Comment on the morphology of the erythrocytes.
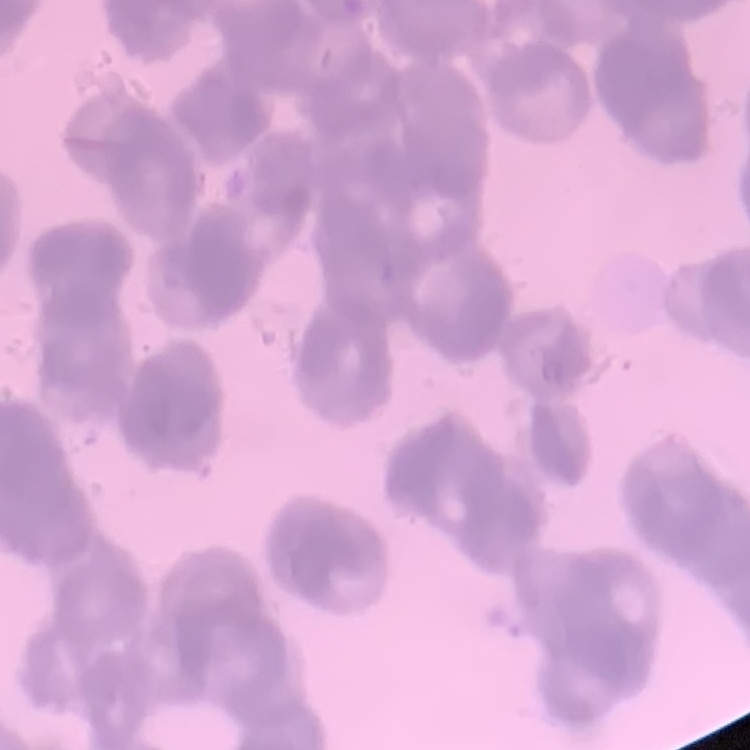

Rouleaux formation.

Thin blood smear. Stained with either Field's or Giemsa. Square crop of a larger photomicrograph.